State which parasite is depicted.
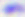

Toxoplasma gondii.

modality = photomicrograph
magnification = 400x